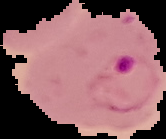

Summary:
  - Image size: 166×139 pixels
  - Preparation: thin blood film
  - Image type: segmented cell region on a black background
  - Malaria status: parasitized